Name the parasite shown.
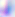
Toxoplasma gondii.

Captured at 400x magnification. Micrograph.